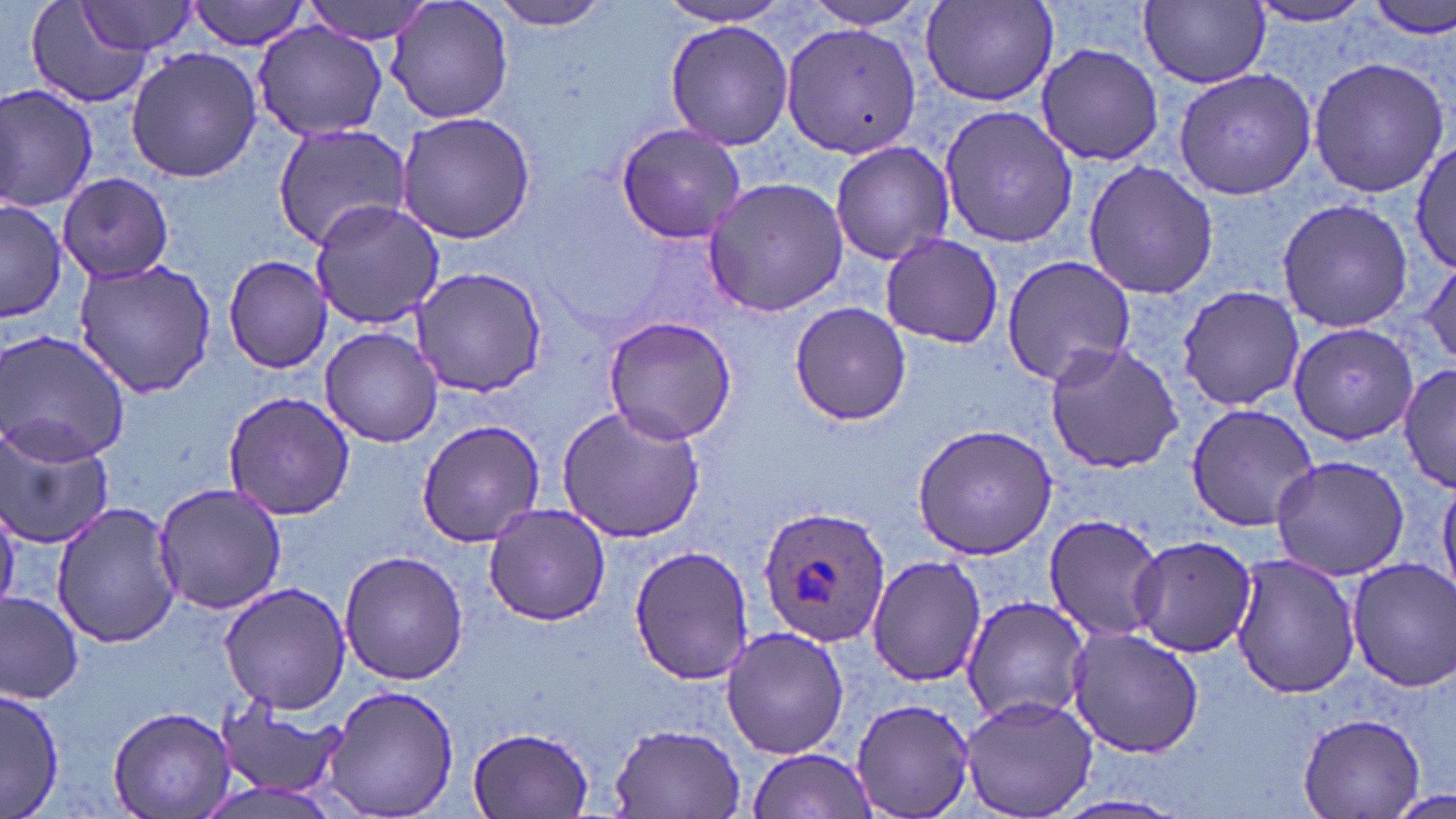

Summary:
  - Coordinate format: approximate bounding boxes as (x1,y1)-(x2,y2) corner pairs in pixels
  - Plasmodium ovale-infected red blood cell locations: (758,503)-(891,648)
  - Uninfected red blood cell locations: (25,0)-(154,109), (187,0)-(310,51), (301,0)-(437,44), (385,0)-(515,126), (486,0)-(620,31), (795,0)-(938,30), (919,0)-(1059,106), (1368,0)-(1455,39), (1245,1)-(1378,27), (78,2)-(198,56), (1141,2)-(1269,88), (655,3)-(795,27), (250,19)-(390,143), (665,21)-(794,148), (781,22)-(922,158), (1034,42)-(1166,167), (124,49)-(263,181), (1306,54)-(1450,200), (1173,67)-(1317,199), (1,83)-(99,212), (939,103)-(1078,249), (396,110)-(538,244), (613,122)-(746,243), (273,124)-(412,248), (1412,137)-(1455,276), (830,140)-(954,266), (1082,161)-(1217,301), (59,172)-(175,282), (701,177)-(849,318), (1276,199)-(1414,332), (1,200)-(69,324), (308,201)-(446,330), (879,235)-(1002,350), (222,253)-(332,374), (1001,253)-(1135,385), (73,257)-(221,399), (1419,259)-(1456,369), (410,266)-(546,396), (1175,284)-(1306,414), (789,302)-(912,426), (602,314)-(739,445), (1289,320)-(1421,445), (321,325)-(443,447), (1,327)-(131,467), (1041,341)-(1185,474), (1396,360)-(1456,490), (223,390)-(355,520), (554,400)-(705,544), (1185,403)-(1319,532), (0,418)-(114,548), (416,419)-(546,547), (911,423)-(1059,560), (1268,454)-(1412,580), (1439,480)-(1456,596), (153,481)-(287,616), (51,502)-(185,650), (483,503)-(614,625), (0,504)-(22,611), (1043,512)-(1169,643), (1126,534)-(1258,658), (630,546)-(756,684), (339,551)-(470,684), (1230,553)-(1360,698), (867,555)-(988,686), (1347,558)-(1456,692), (219,582)-(351,716), (0,590)-(84,703), (961,596)-(1092,725), (720,625)-(850,760), (1066,625)-(1207,759), (323,683)-(461,818), (2,687)-(63,818), (959,695)-(1100,819), (851,696)-(978,819), (214,699)-(344,802), (108,704)-(234,818), (1297,710)-(1427,818), (606,721)-(749,817), (465,725)-(596,817), (746,747)-(878,817), (1390,787)-(1454,819)
  - Slide-level diagnosis: Plasmodium ovale
  - Image size: 1456×819 pixels
  - Magnification: 1000x
  - Modality: optical microscopy
  - Stain: May-Grünwald-Giemsa
  - Field of view: single
  - Preparation: thin blood smear